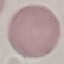

result = no malaria parasites detected
image type = cell patch, automatically extracted from a larger field of view and resized to 64 × 64 pixels
capture = smartphone camera at the microscope eyepiece
preparation = thin blood smear
stain = Giemsa